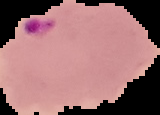
Summary:
  - Image size: 160×115 pixels
  - Preparation: thin blood film
  - Result: malaria parasites identified
  - Image type: segmented cell region with the area outside set to black